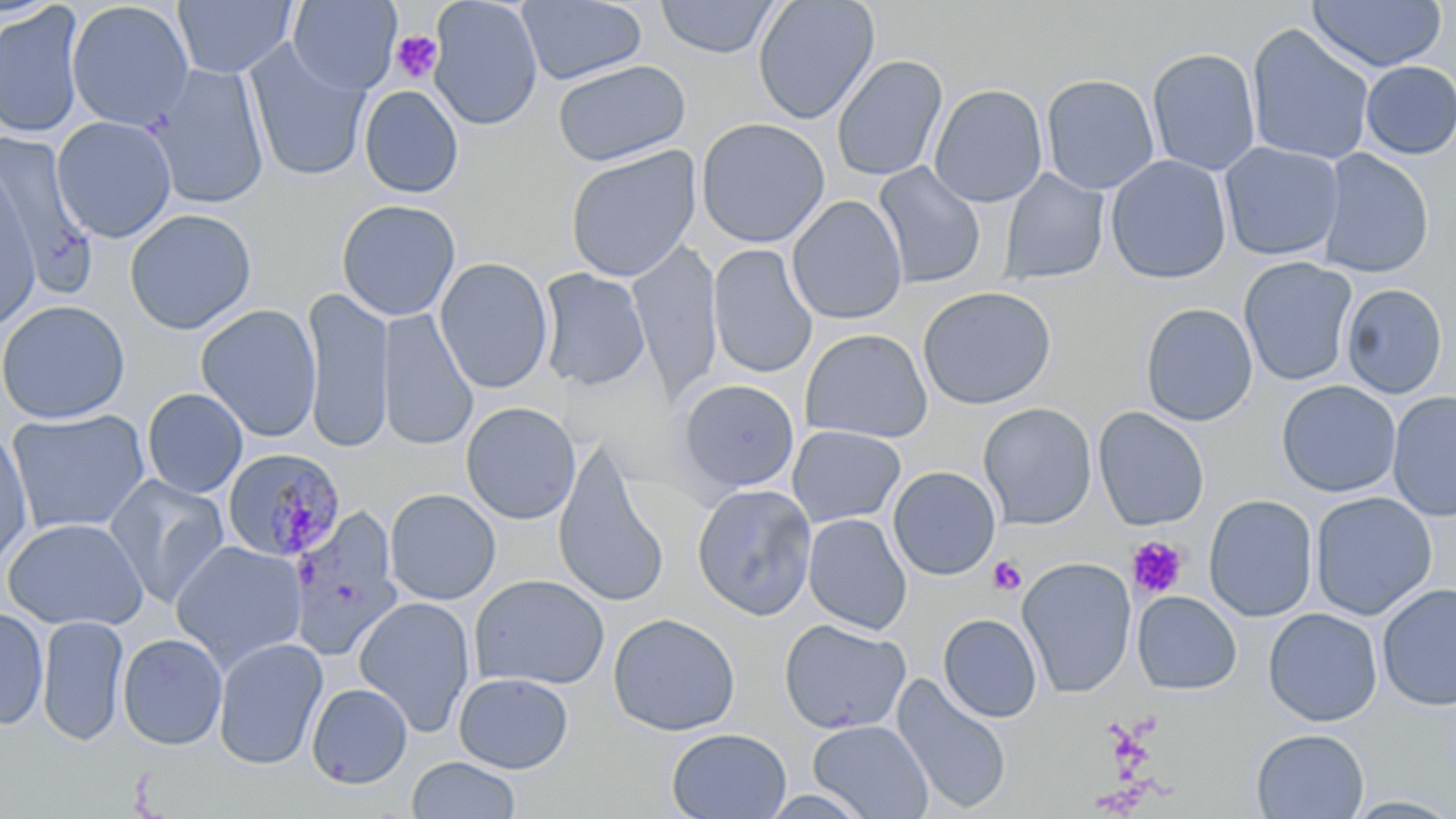

Summary:
  - Coordinate format: approximate bounding boxes as named x1/y1/x2/y2 corners in pixels
  - Platelet locations: (x1=391, y1=30, x2=444, y2=84), (x1=1128, y1=535, x2=1187, y2=599), (x1=988, y1=556, x2=1027, y2=596)
  - Uninfected red blood cell locations: (x1=173, y1=0, x2=298, y2=78), (x1=288, y1=0, x2=401, y2=94), (x1=428, y1=0, x2=544, y2=131), (x1=516, y1=0, x2=648, y2=85), (x1=655, y1=0, x2=780, y2=59), (x1=752, y1=0, x2=879, y2=124), (x1=1308, y1=0, x2=1447, y2=72), (x1=66, y1=1, x2=194, y2=131), (x1=0, y1=4, x2=85, y2=140), (x1=1245, y1=23, x2=1376, y2=167), (x1=244, y1=41, x2=371, y2=182), (x1=1147, y1=47, x2=1261, y2=176), (x1=832, y1=54, x2=948, y2=181), (x1=552, y1=60, x2=691, y2=167), (x1=1360, y1=61, x2=1456, y2=159), (x1=150, y1=63, x2=270, y2=209), (x1=1041, y1=73, x2=1160, y2=195), (x1=929, y1=83, x2=1048, y2=207), (x1=359, y1=84, x2=465, y2=198), (x1=51, y1=115, x2=177, y2=243), (x1=695, y1=117, x2=831, y2=248), (x1=0, y1=132, x2=95, y2=283), (x1=1219, y1=141, x2=1345, y2=262), (x1=564, y1=146, x2=702, y2=282), (x1=1317, y1=149, x2=1434, y2=278), (x1=1105, y1=155, x2=1232, y2=285), (x1=873, y1=162, x2=987, y2=288), (x1=0, y1=163, x2=41, y2=331), (x1=999, y1=168, x2=1109, y2=286), (x1=787, y1=195, x2=908, y2=325), (x1=336, y1=199, x2=461, y2=321), (x1=124, y1=208, x2=257, y2=335), (x1=628, y1=242, x2=724, y2=404), (x1=708, y1=244, x2=818, y2=380), (x1=1238, y1=256, x2=1358, y2=387), (x1=434, y1=257, x2=554, y2=394), (x1=538, y1=268, x2=651, y2=392), (x1=1340, y1=283, x2=1448, y2=399), (x1=917, y1=285, x2=1057, y2=410), (x1=301, y1=286, x2=394, y2=454), (x1=0, y1=299, x2=130, y2=424), (x1=1140, y1=303, x2=1258, y2=426), (x1=196, y1=304, x2=322, y2=442), (x1=377, y1=309, x2=478, y2=451), (x1=800, y1=328, x2=933, y2=444), (x1=676, y1=379, x2=800, y2=495), (x1=1276, y1=380, x2=1401, y2=497), (x1=142, y1=388, x2=248, y2=498), (x1=1387, y1=390, x2=1456, y2=523), (x1=460, y1=402, x2=581, y2=524), (x1=978, y1=402, x2=1097, y2=530), (x1=1093, y1=407, x2=1210, y2=531), (x1=5, y1=408, x2=151, y2=536), (x1=787, y1=425, x2=906, y2=527), (x1=0, y1=426, x2=34, y2=569), (x1=552, y1=443, x2=672, y2=607), (x1=888, y1=466, x2=1001, y2=580), (x1=103, y1=474, x2=230, y2=608), (x1=692, y1=482, x2=817, y2=619), (x1=384, y1=488, x2=501, y2=605), (x1=1310, y1=491, x2=1437, y2=620), (x1=1204, y1=494, x2=1318, y2=622), (x1=289, y1=508, x2=403, y2=661), (x1=803, y1=513, x2=912, y2=635), (x1=1, y1=517, x2=148, y2=630), (x1=169, y1=540, x2=307, y2=671), (x1=1017, y1=557, x2=1137, y2=698), (x1=469, y1=574, x2=610, y2=690), (x1=1377, y1=582, x2=1456, y2=712), (x1=1132, y1=590, x2=1242, y2=694), (x1=353, y1=596, x2=475, y2=737), (x1=0, y1=606, x2=49, y2=731), (x1=1263, y1=607, x2=1383, y2=726), (x1=607, y1=612, x2=741, y2=736), (x1=938, y1=613, x2=1042, y2=723), (x1=36, y1=614, x2=129, y2=745), (x1=778, y1=618, x2=911, y2=735), (x1=117, y1=632, x2=228, y2=751), (x1=213, y1=637, x2=328, y2=770), (x1=453, y1=672, x2=574, y2=774), (x1=891, y1=672, x2=1013, y2=815), (x1=306, y1=682, x2=413, y2=789), (x1=808, y1=719, x2=933, y2=819), (x1=667, y1=727, x2=791, y2=819), (x1=1251, y1=728, x2=1369, y2=818), (x1=407, y1=756, x2=521, y2=818), (x1=1341, y1=795, x2=1456, y2=818)
  - Plasmodium malariae-infected red blood cell locations: (x1=222, y1=449, x2=349, y2=564)
  - Slide-level diagnosis: Plasmodium malariae
  - Preparation: thin blood smear
  - Modality: light microscopy
  - Image size: 1456×819 pixels
  - Magnification: 1000x
  - Field of view: single
  - Stain: May-Grünwald-Giemsa